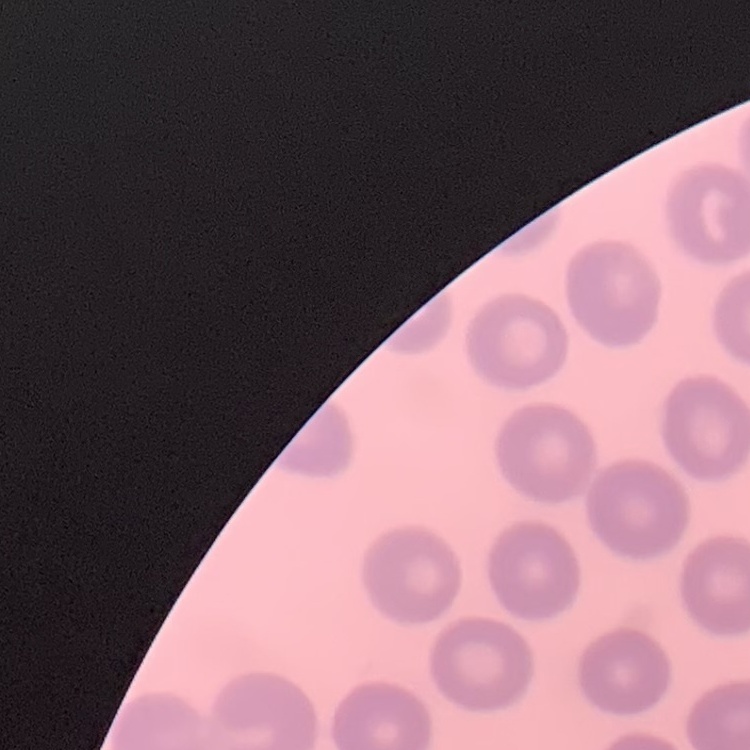

red blood cell morphology = no rouleaux formation
stain = Field's or Giemsa
preparation = thin blood film
image type = one tile cut from a larger photomicrograph